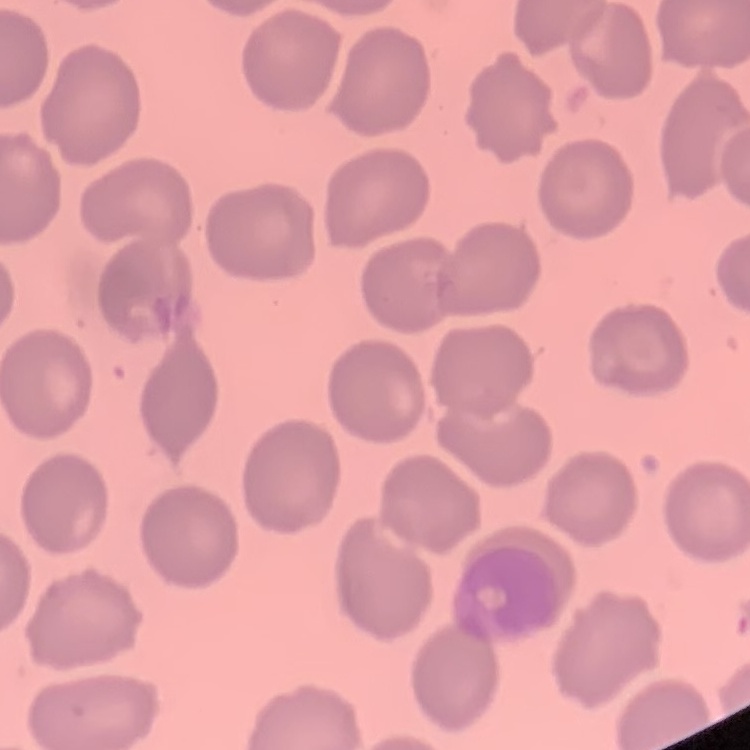
Summary:
  - Red blood cell morphology: no rouleaux formation
  - Preparation: thin peripheral smear
  - Stain: Field's or Giemsa
  - Image type: one tile cut from a larger photomicrograph